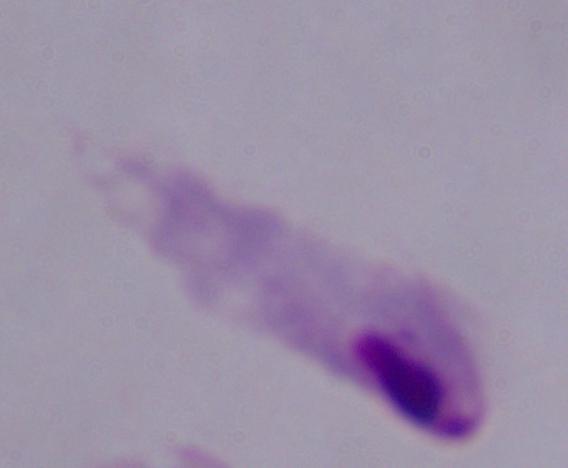
modality = photomicrograph
identification = trichomonad
magnification = 1000x